Assess this cell for malaria.
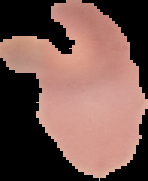

It is uninfected.

Summary:
  - Image type: segmented cell region on a black background
  - Image size: 148×181 pixels
  - Preparation: thin blood film